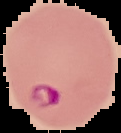 Image is 121×133 pixels. From a thin blood smear. Result: malaria parasites identified. The area outside the segmented cell region is set to black.